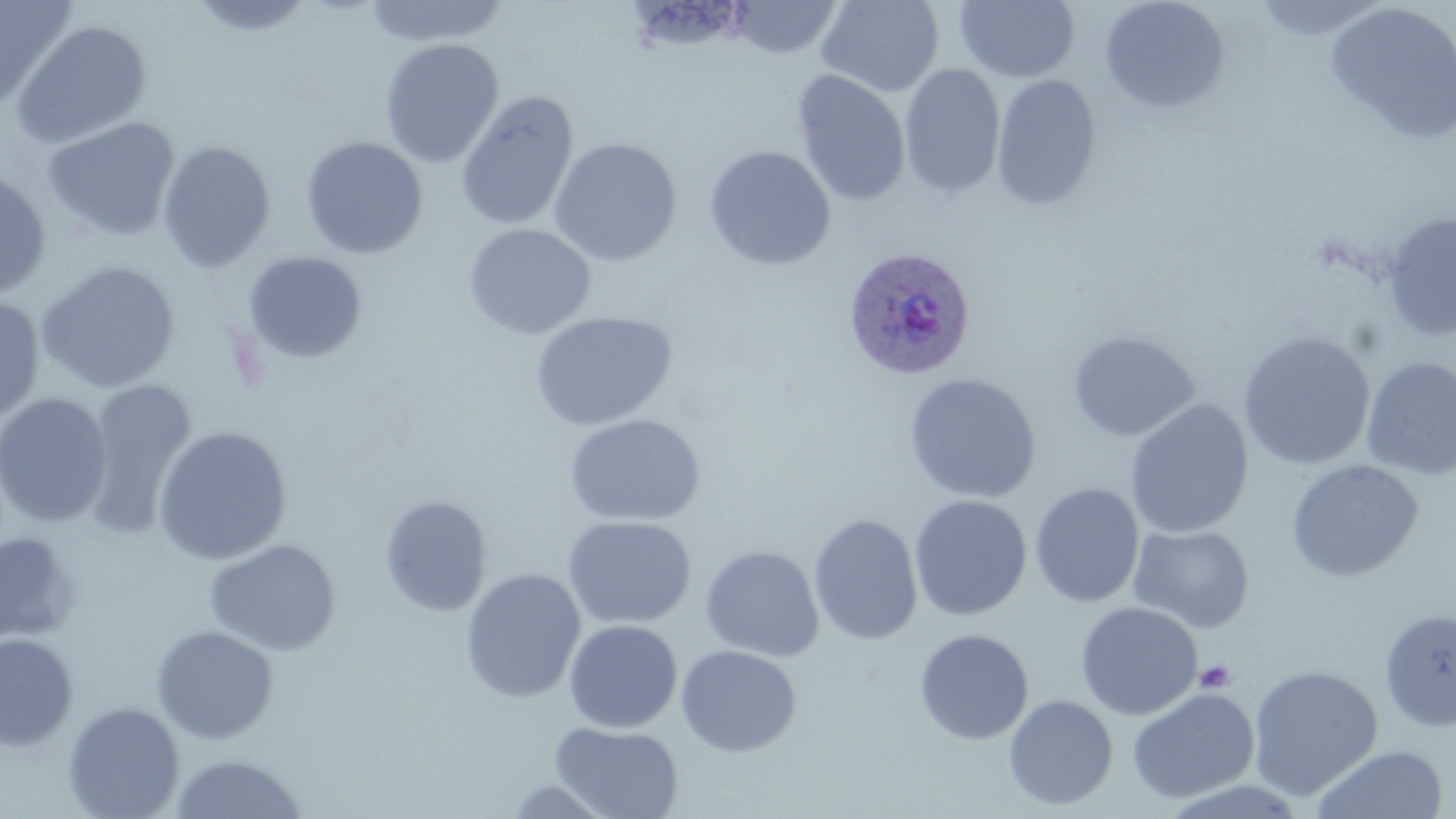 Approximate bounding boxes as named x1/y1/x2/y2 corners in pixels. Platelet locations: (x1=1194, y1=660, x2=1236, y2=693). Plasmodium ovale-infected red blood cell locations: (x1=842, y1=245, x2=975, y2=380). Uninfected red blood cell locations: (x1=187, y1=0, x2=317, y2=38), (x1=361, y1=0, x2=508, y2=48), (x1=728, y1=0, x2=844, y2=59), (x1=815, y1=0, x2=944, y2=97), (x1=954, y1=0, x2=1080, y2=83), (x1=1098, y1=0, x2=1230, y2=114), (x1=1252, y1=0, x2=1393, y2=42), (x1=0, y1=1, x2=76, y2=111), (x1=1324, y1=1, x2=1456, y2=143), (x1=11, y1=20, x2=152, y2=150), (x1=379, y1=38, x2=503, y2=168), (x1=898, y1=64, x2=1006, y2=199), (x1=790, y1=70, x2=911, y2=207), (x1=991, y1=74, x2=1102, y2=211), (x1=454, y1=90, x2=578, y2=231), (x1=41, y1=116, x2=181, y2=242), (x1=300, y1=137, x2=428, y2=260), (x1=548, y1=137, x2=682, y2=266), (x1=156, y1=141, x2=276, y2=272), (x1=703, y1=145, x2=836, y2=270), (x1=0, y1=168, x2=52, y2=300), (x1=1381, y1=212, x2=1456, y2=341), (x1=463, y1=223, x2=596, y2=340), (x1=241, y1=251, x2=367, y2=364), (x1=35, y1=261, x2=181, y2=393), (x1=0, y1=297, x2=45, y2=426), (x1=529, y1=310, x2=677, y2=432), (x1=1067, y1=330, x2=1200, y2=442), (x1=1238, y1=332, x2=1376, y2=471), (x1=1360, y1=356, x2=1456, y2=481), (x1=903, y1=373, x2=1041, y2=504), (x1=79, y1=377, x2=197, y2=539), (x1=0, y1=393, x2=113, y2=529), (x1=1124, y1=399, x2=1254, y2=539), (x1=564, y1=413, x2=705, y2=526), (x1=151, y1=426, x2=292, y2=565), (x1=1286, y1=459, x2=1423, y2=583), (x1=1029, y1=483, x2=1145, y2=608), (x1=379, y1=495, x2=492, y2=617), (x1=909, y1=495, x2=1032, y2=621), (x1=808, y1=513, x2=923, y2=645), (x1=562, y1=515, x2=696, y2=629), (x1=1127, y1=524, x2=1255, y2=634), (x1=0, y1=532, x2=80, y2=646), (x1=203, y1=539, x2=341, y2=656), (x1=700, y1=544, x2=824, y2=661), (x1=459, y1=568, x2=586, y2=703), (x1=1075, y1=601, x2=1203, y2=720), (x1=1379, y1=607, x2=1456, y2=733), (x1=563, y1=620, x2=683, y2=733), (x1=150, y1=625, x2=279, y2=743), (x1=914, y1=628, x2=1034, y2=745), (x1=0, y1=634, x2=78, y2=753), (x1=675, y1=644, x2=802, y2=756), (x1=1247, y1=664, x2=1383, y2=801), (x1=1126, y1=687, x2=1260, y2=804), (x1=1002, y1=694, x2=1118, y2=810), (x1=62, y1=701, x2=185, y2=819), (x1=549, y1=722, x2=684, y2=819), (x1=1309, y1=743, x2=1449, y2=819), (x1=168, y1=753, x2=309, y2=818), (x1=500, y1=778, x2=619, y2=818). Slide-level diagnosis: Plasmodium ovale. 1000x magnification. Image is 1456×819 pixels. Thin blood smear. May-Grünwald-Giemsa-stained preparation. Optical microscopy. Single field of view.